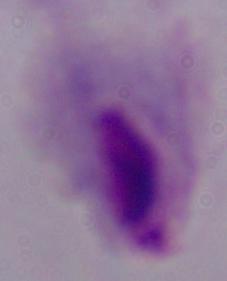

Captured at 1000x magnification. Photomicrograph. A trichomonad is seen.